Report the malaria status of this cell.
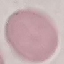

It is uninfected.

preparation = thin smear
stain = Giemsa
capture = smartphone through the microscope eyepiece
image type = cell patch, automatically extracted from a larger field of view and resized to 64 × 64 pixels